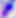

Summary:
  - Identification: Toxoplasma gondii
  - Modality: micrograph
  - Magnification: 400x